State the blood parasite species.
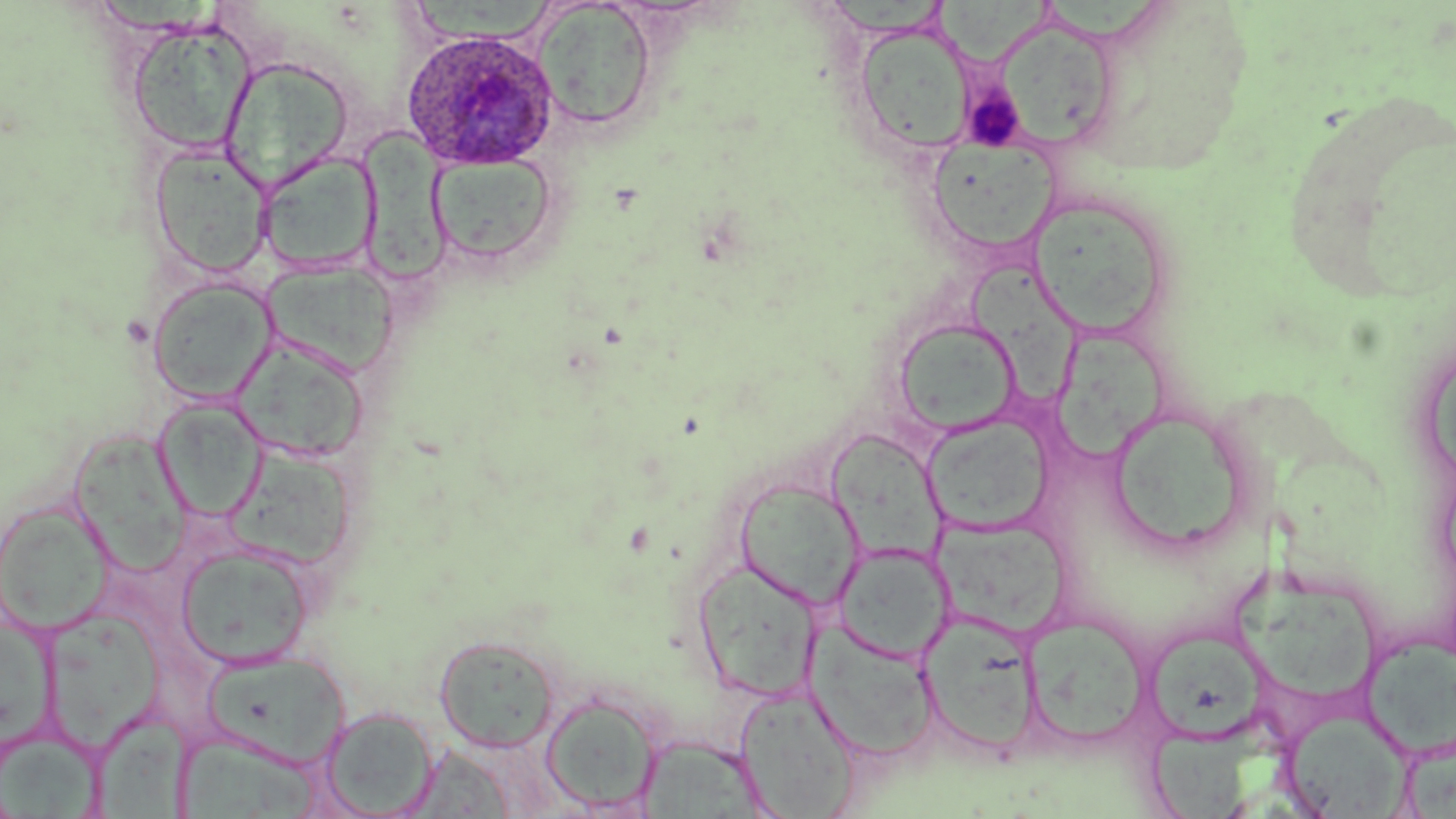

Plasmodium ovale.

Summary:
  - Coordinate format: approximate bounding boxes as [x1, y1, x2, y2] in pixels
  - Platelet locations: [963, 86, 1025, 150]
  - Uninfected red blood cell locations: [413, 0, 556, 45], [932, 0, 1052, 66], [533, 2, 657, 130], [997, 15, 1119, 152], [126, 17, 257, 158], [856, 24, 975, 155], [220, 55, 354, 190], [363, 125, 457, 288], [933, 139, 1060, 253], [148, 144, 274, 279], [257, 151, 381, 275], [428, 153, 559, 270], [1031, 206, 1168, 338], [969, 261, 1077, 404], [261, 262, 399, 378], [147, 276, 277, 405], [894, 321, 1027, 438], [1054, 332, 1170, 466], [233, 336, 369, 464], [152, 398, 268, 521], [1105, 405, 1258, 556], [922, 413, 1055, 534], [78, 432, 196, 572], [823, 432, 952, 564], [224, 447, 357, 569], [733, 480, 866, 612], [0, 500, 115, 636], [937, 519, 1069, 639], [832, 542, 953, 664], [176, 543, 314, 669], [692, 556, 824, 703], [1232, 573, 1381, 702], [50, 609, 166, 757], [920, 613, 1043, 757], [1020, 613, 1152, 750], [1, 617, 66, 755], [1144, 617, 1272, 747], [807, 626, 939, 761], [434, 633, 560, 753], [1363, 635, 1456, 755], [200, 649, 350, 769], [734, 687, 860, 818], [541, 693, 661, 814], [320, 706, 439, 817], [91, 708, 194, 819], [1280, 711, 1411, 815], [1152, 715, 1282, 819], [180, 721, 336, 819], [3, 727, 111, 819], [637, 735, 769, 818], [405, 744, 519, 818]
  - Plasmodium ovale-infected red blood cell locations: [401, 27, 563, 173]
  - Field of view: one of a larger specimen
  - Image size: 1456×819 pixels
  - Preparation: thin blood film
  - Stain: May-Grünwald-Giemsa
  - Magnification: 1000x
  - Modality: optical microscopy